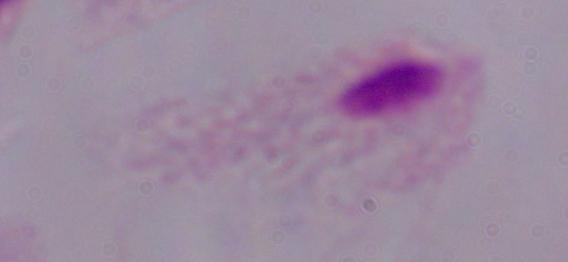

Summary:
  - Magnification: 1000x
  - Identification: trichomonad
  - Modality: photomicrograph